Locate every Plasmodium ovale-infected red blood cell.
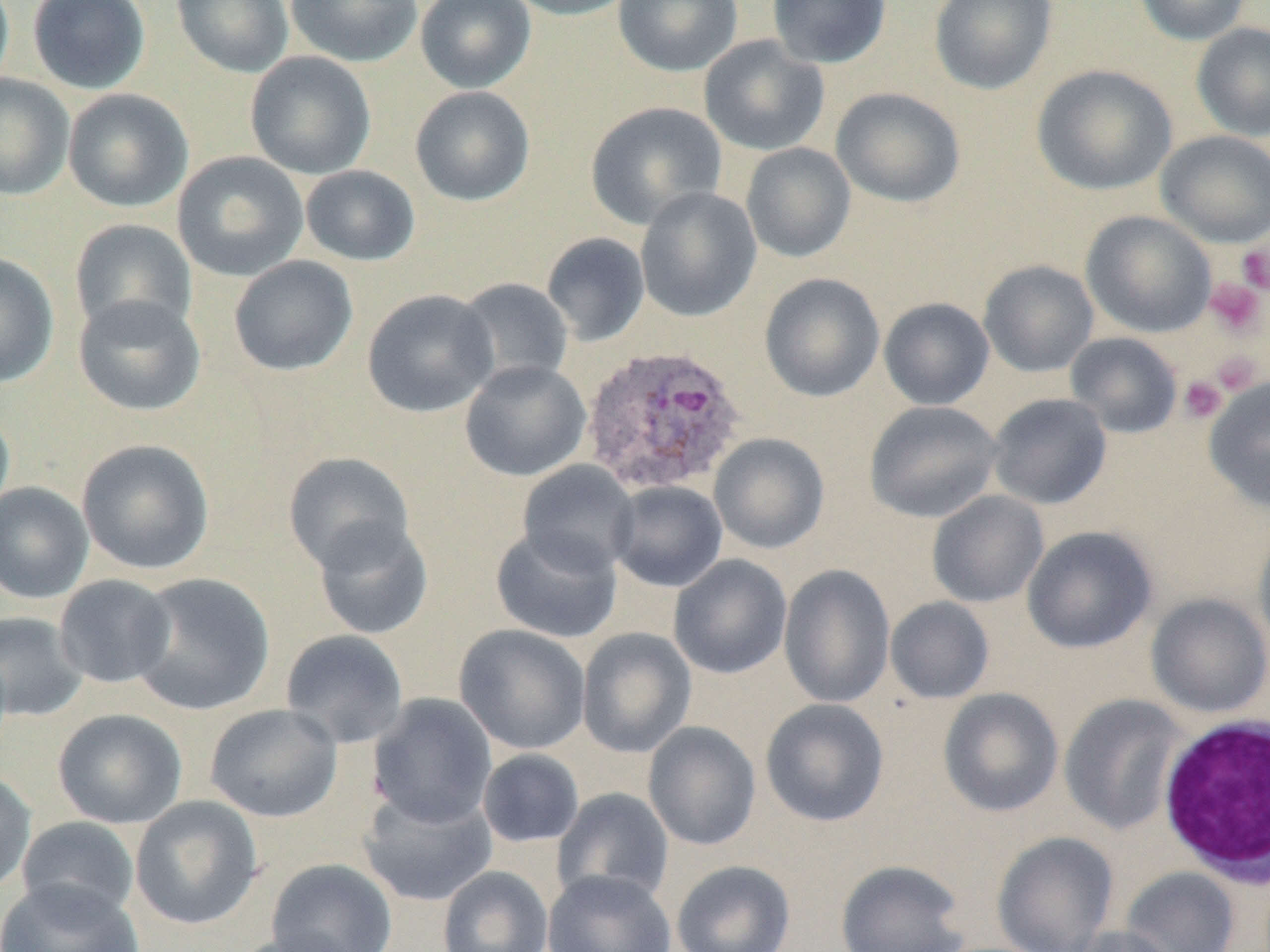
Approximate bounding boxes as (x1,y1)-(x2,y2) corner pairs in pixels.
Plasmodium ovale-infected red blood cells: (581,343)-(747,495).

Summary:
  - White blood cell locations: (1157,713)-(1270,888)
  - Platelet locations: (1236,242)-(1270,294), (1204,278)-(1266,338), (1210,351)-(1263,395), (1178,376)-(1228,424)
  - Uninfected red blood cell locations: (27,0)-(151,94), (172,0)-(294,78), (285,0)-(423,67), (415,0)-(536,93), (503,0)-(637,20), (612,0)-(743,76), (767,0)-(891,69), (928,0)-(1058,95), (1134,0)-(1253,46), (1191,22)-(1270,142), (698,35)-(830,157), (245,51)-(376,180), (1032,64)-(1177,195), (0,73)-(75,201), (409,86)-(535,206), (830,86)-(966,208), (63,88)-(194,213), (585,101)-(728,230), (1155,130)-(1270,248), (741,142)-(856,262), (172,151)-(309,281), (300,165)-(420,267), (635,187)-(762,322), (1080,210)-(1217,338), (69,218)-(198,339), (541,232)-(650,346), (0,252)-(60,388), (228,256)-(359,377), (978,260)-(1099,377), (759,273)-(885,402), (455,278)-(574,390), (362,288)-(500,417), (73,294)-(207,416), (878,298)-(995,410), (1065,332)-(1183,439), (460,360)-(591,482), (1203,378)-(1270,512), (987,393)-(1112,510), (864,400)-(1003,523), (0,404)-(15,523), (709,432)-(830,554), (76,438)-(215,576), (283,452)-(415,572), (517,460)-(640,576), (608,480)-(728,592), (0,482)-(94,604), (927,491)-(1048,607), (312,516)-(434,640), (1253,518)-(1270,656), (1021,525)-(1157,654), (491,526)-(623,643), (668,554)-(793,679), (778,564)-(896,709), (129,572)-(277,715), (53,575)-(177,689), (1146,592)-(1270,718), (885,596)-(995,704), (0,611)-(88,722), (454,624)-(592,755), (576,627)-(697,759), (280,629)-(409,748), (938,688)-(1064,817), (367,693)-(498,828), (1059,694)-(1188,835), (760,698)-(890,827), (204,703)-(342,823), (52,708)-(187,829), (642,721)-(761,851), (478,748)-(584,848), (0,768)-(36,894), (552,787)-(674,906), (358,790)-(497,906), (130,796)-(263,930), (16,816)-(140,922), (991,831)-(1119,952), (266,858)-(398,952), (671,860)-(796,952), (834,860)-(971,952), (436,865)-(553,952), (1121,867)-(1240,952), (543,868)-(678,952), (0,879)-(145,952), (1064,925)-(1182,952), (227,930)-(364,952)
  - Slide-level diagnosis: Plasmodium ovale
  - Magnification: 1000x
  - Modality: optical microscopy
  - Preparation: thin blood film
  - Image size: 1270×952 pixels
  - Field of view: one of a larger specimen